Assess this cell for malaria.
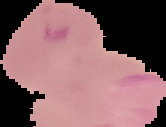

It is parasitized.

preparation = thin blood film
image type = segmented cell region with the area outside set to black
image size = 166×127 pixels